Locate every leukocyte (white blood cell).
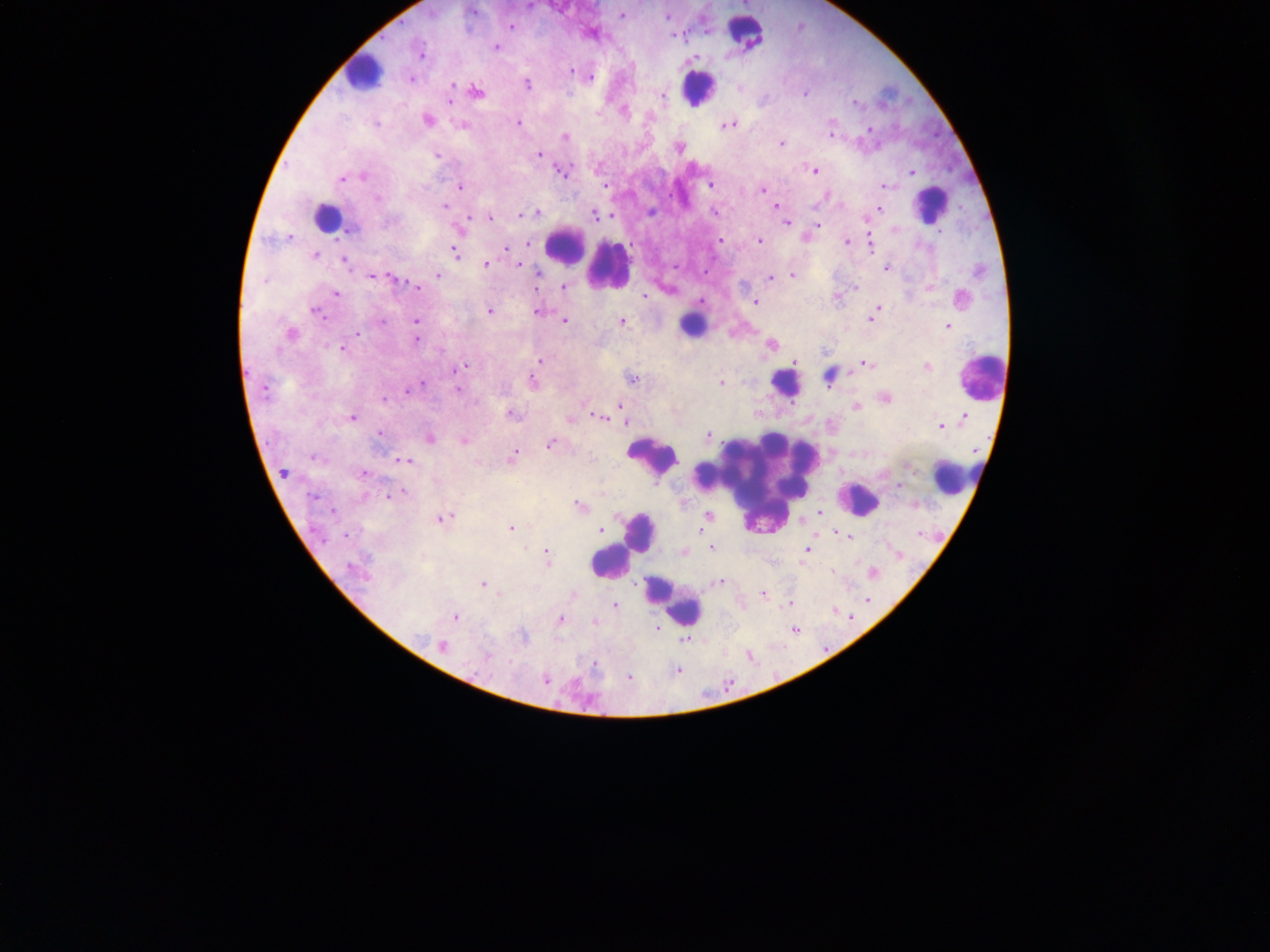
Approximate centers as (x, y) in pixels.
Leukocytes: (747, 33), (362, 72), (698, 90), (932, 205), (327, 218), (565, 248), (607, 268), (691, 327), (983, 382), (785, 384), (652, 457), (951, 480), (755, 483), (858, 503), (641, 533), (610, 564), (673, 602).

Malaria parasite locations: (745, 5), (623, 17), (668, 18), (512, 28), (685, 36), (497, 48), (422, 58), (693, 60), (589, 78), (412, 81), (453, 85), (527, 85), (477, 94), (805, 95), (663, 98), (450, 102), (856, 104), (624, 113), (428, 122), (519, 124), (729, 127), (868, 129), (831, 134), (565, 139), (782, 145), (679, 149), (540, 156), (438, 157), (813, 171), (912, 173), (562, 174), (363, 177), (343, 180), (711, 186), (460, 187), (608, 187), (885, 187), (763, 191), (828, 195), (776, 207), (446, 208), (879, 210), (538, 213), (716, 213), (875, 214), (521, 216), (596, 217), (490, 219), (788, 224), (818, 226), (290, 241), (719, 241), (760, 242), (530, 243), (846, 243), (870, 245), (506, 251), (455, 253), (315, 258), (345, 262), (487, 266), (519, 266), (887, 269), (372, 276), (438, 276), (537, 276), (793, 276), (771, 279), (394, 281), (564, 287), (417, 288), (854, 288), (336, 294), (647, 298), (838, 299), (702, 303), (756, 304), (876, 311), (490, 313), (538, 314), (318, 316), (871, 320), (417, 321), (566, 323), (622, 323), (948, 328), (292, 335), (416, 340), (772, 346), (344, 351), (541, 360), (795, 363), (865, 365), (464, 367), (927, 368), (460, 369), (633, 380), (830, 380), (534, 384), (723, 384), (423, 385), (407, 392), (458, 392), (886, 400), (385, 401), (857, 408), (621, 409), (512, 416), (624, 417), (601, 418), (353, 419), (964, 419), (570, 421), (624, 423), (942, 427), (380, 434), (709, 437), (431, 440), (465, 442), (551, 446), (514, 459), (313, 460), (404, 461), (284, 475), (364, 475), (899, 488), (403, 493), (315, 500), (580, 508), (334, 512), (819, 513), (708, 519), (445, 520), (511, 529), (600, 532), (838, 535), (712, 549), (808, 552), (685, 553), (898, 557), (547, 558), (873, 575), (361, 576), (722, 583), (484, 586), (574, 595), (764, 595), (868, 600), (790, 605), (616, 607), (844, 615), (455, 618), (560, 621), (597, 622), (657, 629), (795, 633), (524, 637), (684, 640), (443, 648), (751, 658), (678, 672), (629, 679), (546, 681). Sample from Ghana. Single field of view. Thick blood film. Image is 1270×952 pixels. Mobile-phone photograph taken through the microscope.